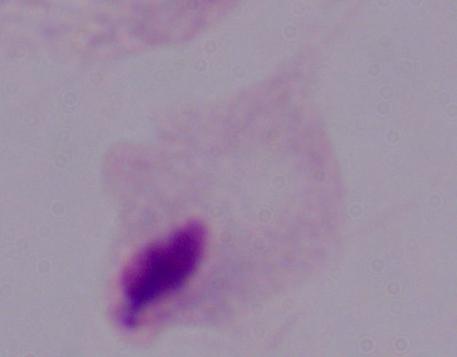
Summary:
  - Modality: photomicrograph
  - Identification: trichomonad
  - Magnification: 1000x